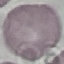 Malaria status: uninfected. Thin blood smear. Photographed with a smartphone camera at the microscope eyepiece. Cell patch, automatically extracted from a larger field of view and resized to 64 × 64 pixels. Giemsa stain.